Give the extent of all Plasmodium malariae-infected red blood cells.
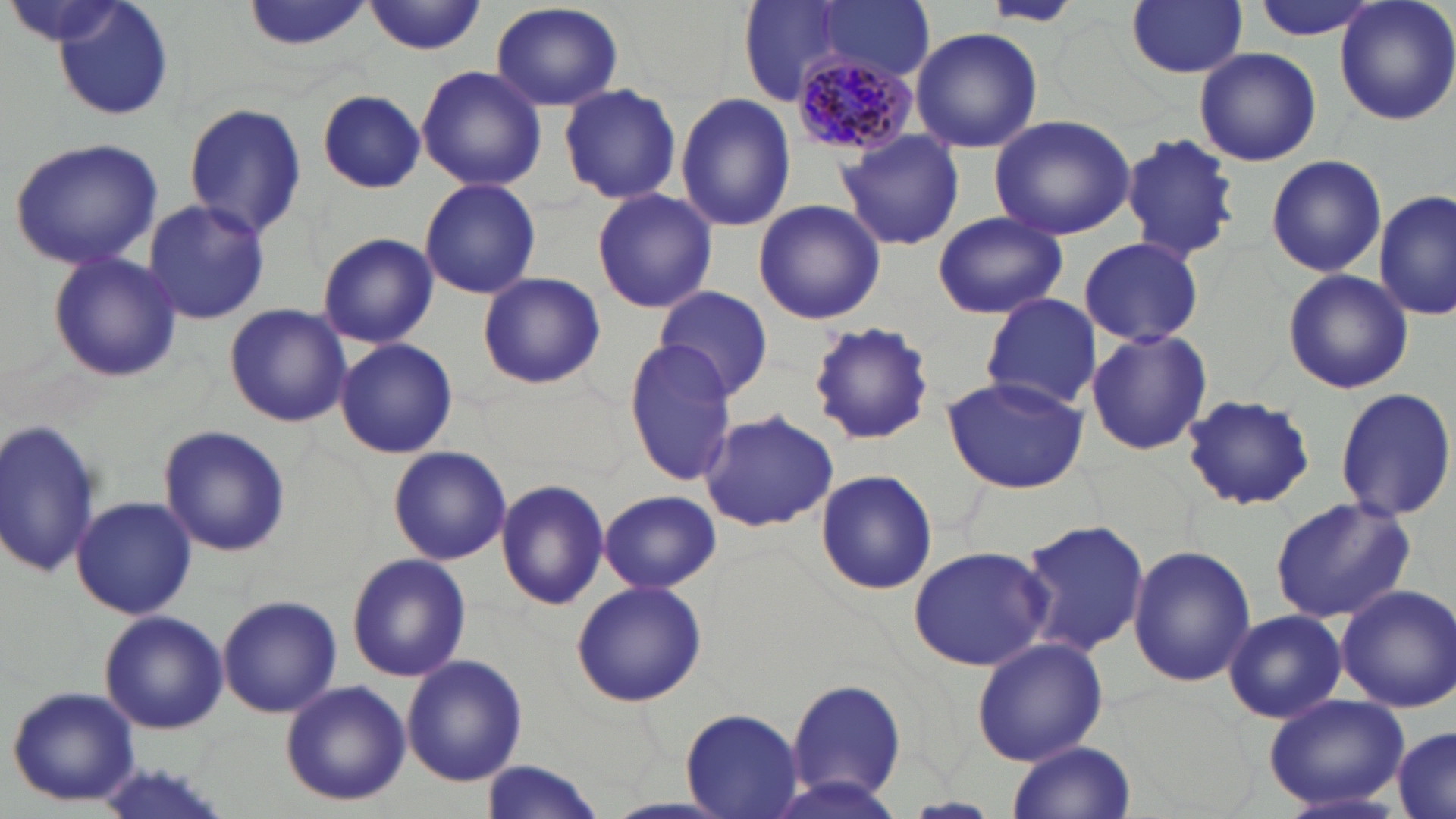
Approximate bounding boxes as (x1, y1, x2, y2) in pixels.
Plasmodium malariae-infected red blood cells: (790, 46, 921, 159).

Summary:
  - Uninfected red blood cell locations: (50, 0, 175, 122), (240, 0, 375, 52), (364, 0, 485, 55), (818, 0, 936, 78), (1127, 0, 1248, 78), (1251, 0, 1384, 41), (1333, 0, 1456, 125), (489, 2, 624, 112), (980, 2, 1087, 28), (733, 3, 870, 105), (910, 27, 1044, 154), (1194, 48, 1322, 168), (415, 65, 547, 191), (558, 82, 682, 205), (316, 89, 426, 193), (675, 92, 796, 231), (183, 101, 306, 239), (988, 114, 1137, 241), (834, 128, 963, 251), (1121, 132, 1243, 263), (8, 137, 163, 270), (1265, 154, 1387, 278), (419, 178, 542, 300), (591, 188, 718, 314), (1375, 189, 1455, 322), (142, 199, 271, 323), (753, 199, 885, 324), (933, 212, 1066, 319), (316, 232, 439, 349), (1080, 239, 1203, 346), (46, 249, 182, 383), (1282, 269, 1414, 395), (475, 273, 605, 391), (654, 285, 772, 399), (980, 293, 1101, 412), (223, 302, 350, 428), (809, 320, 936, 444), (1085, 327, 1213, 456), (334, 337, 458, 459), (623, 341, 737, 485), (941, 375, 1091, 494), (1333, 385, 1456, 522), (1180, 392, 1317, 512), (697, 410, 841, 533), (0, 417, 102, 581), (158, 425, 291, 558), (387, 446, 512, 565), (814, 467, 940, 597), (495, 478, 610, 612), (598, 490, 721, 594), (72, 495, 196, 620), (1269, 497, 1415, 624), (1018, 518, 1148, 659), (908, 543, 1055, 671), (1128, 544, 1255, 687), (346, 553, 471, 683), (571, 579, 706, 707), (1335, 583, 1456, 712), (218, 593, 341, 718), (1223, 609, 1348, 723), (98, 610, 228, 734), (972, 637, 1107, 765), (402, 654, 527, 785), (782, 675, 908, 803), (279, 680, 411, 808), (5, 685, 141, 806), (1262, 692, 1409, 811), (681, 705, 806, 817), (1390, 725, 1456, 819), (1006, 740, 1137, 819), (477, 760, 606, 819)
  - Slide-level diagnosis: Plasmodium malariae
  - Modality: light microscopy
  - Field of view: single
  - Preparation: thin blood smear
  - Stain: May-Grünwald-Giemsa
  - Image size: 1456×819 pixels
  - Magnification: 1000x